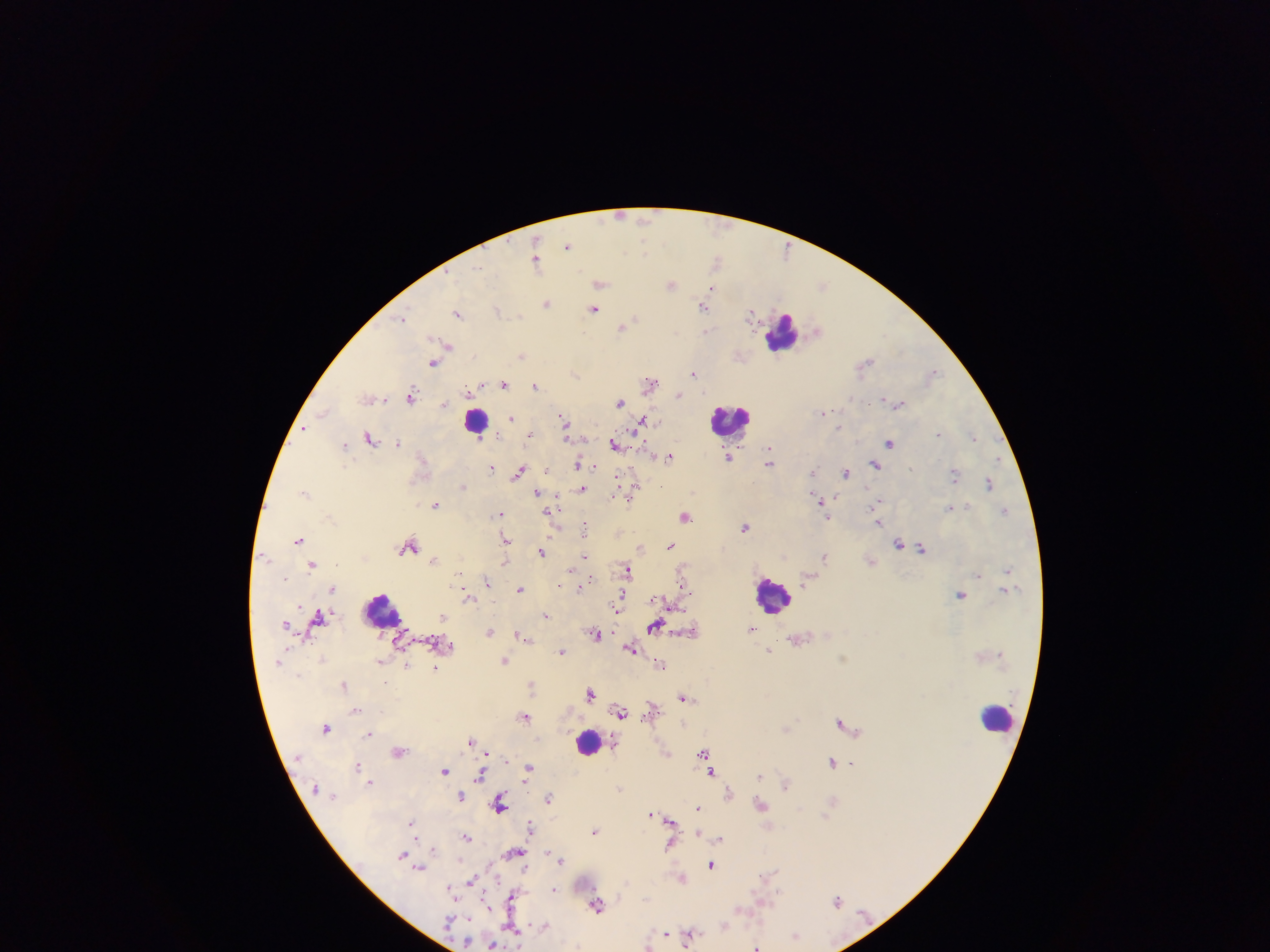

Approximate centers as {x, y} in pixels.
Summary:
  - Leukocyte locations: {784, 332}, {476, 420}, {731, 420}, {771, 595}, {382, 610}, {997, 716}, {589, 741}
  - Malaria parasite locations: {620, 215}, {646, 219}, {568, 246}, {644, 251}, {715, 260}, {536, 261}, {478, 266}, {601, 284}, {670, 284}, {823, 285}, {712, 289}, {547, 303}, {704, 307}, {594, 309}, {497, 310}, {751, 313}, {459, 314}, {403, 317}, {629, 323}, {623, 327}, {707, 330}, {817, 330}, {448, 345}, {522, 355}, {867, 361}, {433, 363}, {934, 372}, {575, 373}, {693, 374}, {503, 383}, {650, 383}, {535, 386}, {679, 395}, {412, 396}, {851, 398}, {883, 399}, {619, 402}, {445, 404}, {899, 404}, {324, 412}, {823, 413}, {510, 418}, {643, 420}, {564, 422}, {839, 427}, {305, 428}, {938, 434}, {531, 435}, {566, 435}, {973, 437}, {371, 438}, {399, 442}, {890, 442}, {615, 443}, {344, 446}, {769, 450}, {670, 457}, {729, 458}, {997, 459}, {769, 462}, {579, 463}, {875, 465}, {491, 469}, {813, 470}, {519, 472}, {847, 472}, {954, 474}, {989, 483}, {462, 488}, {582, 489}, {304, 492}, {536, 492}, {631, 493}, {837, 497}, {820, 501}, {877, 502}, {435, 505}, {950, 508}, {1005, 510}, {499, 514}, {685, 516}, {827, 517}, {879, 522}, {584, 527}, {746, 527}, {299, 539}, {505, 541}, {898, 543}, {670, 545}, {408, 546}, {640, 547}, {922, 548}, {542, 552}, {266, 557}, {585, 557}, {825, 557}, {435, 559}, {505, 559}, {312, 565}, {628, 570}, {1008, 570}, {978, 574}, {286, 579}, {808, 579}, {486, 582}, {682, 584}, {581, 587}, {520, 589}, {333, 590}, {962, 595}, {467, 599}, {620, 600}, {617, 606}, {547, 616}, {320, 618}, {285, 623}, {655, 626}, {753, 629}, {489, 631}, {688, 632}, {595, 635}, {522, 636}, {450, 645}, {630, 649}, {769, 650}, {562, 652}, {505, 660}, {406, 665}, {661, 665}, {435, 668}, {532, 684}, {344, 685}, {591, 694}, {684, 698}, {651, 708}, {356, 710}, {621, 712}, {524, 717}, {841, 721}, {325, 728}, {787, 729}, {369, 734}, {472, 740}, {398, 751}, {703, 752}, {832, 761}, {357, 765}, {444, 770}, {528, 770}, {711, 773}, {480, 774}, {759, 776}, {370, 782}, {785, 783}, {619, 788}, {729, 793}, {461, 796}, {549, 798}, {500, 803}, {761, 804}, {698, 808}, {651, 813}, {670, 821}, {411, 822}, {531, 826}, {595, 831}, {698, 833}, {466, 837}, {720, 839}, {669, 847}, {434, 849}, {514, 852}, {403, 855}, {557, 856}, {561, 860}, {711, 865}, {420, 868}, {770, 873}, {682, 877}, {472, 880}, {554, 889}, {452, 890}, {512, 898}, {837, 901}, {597, 904}, {724, 924}, {544, 926}, {512, 929}, {665, 933}, {691, 934}, {796, 935}, {493, 945}, {757, 946}
  - Capture: mobile-phone photograph through a microscope
  - Image size: 1270×952 pixels
  - Preparation: thick blood film
  - Country: Ghana
  - Field of view: single